Describe the morphology of the erythrocytes.
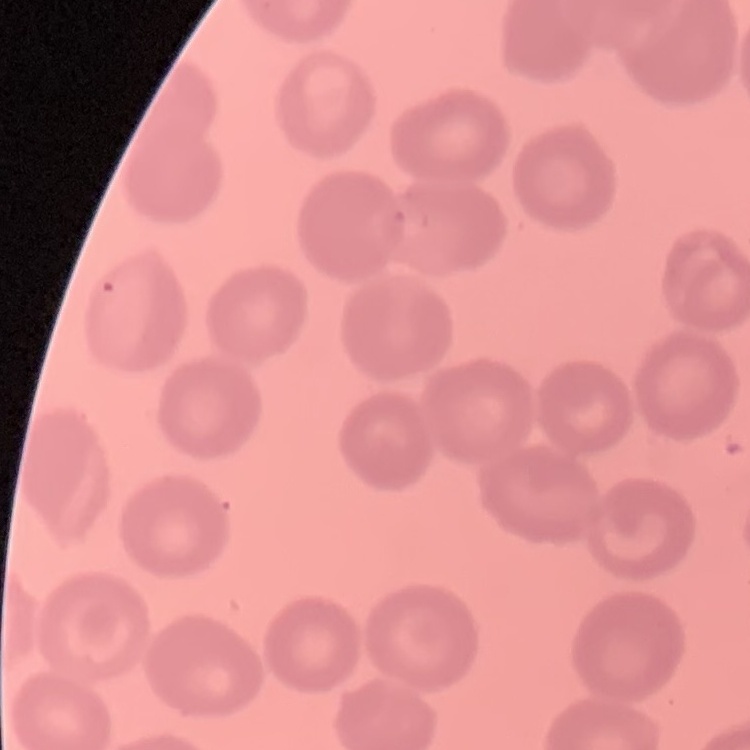

They show no rouleaux formation.

One tile cut from a larger photomicrograph. Field's or Giemsa stain. Thin peripheral smear.